Identify the blood parasite species.
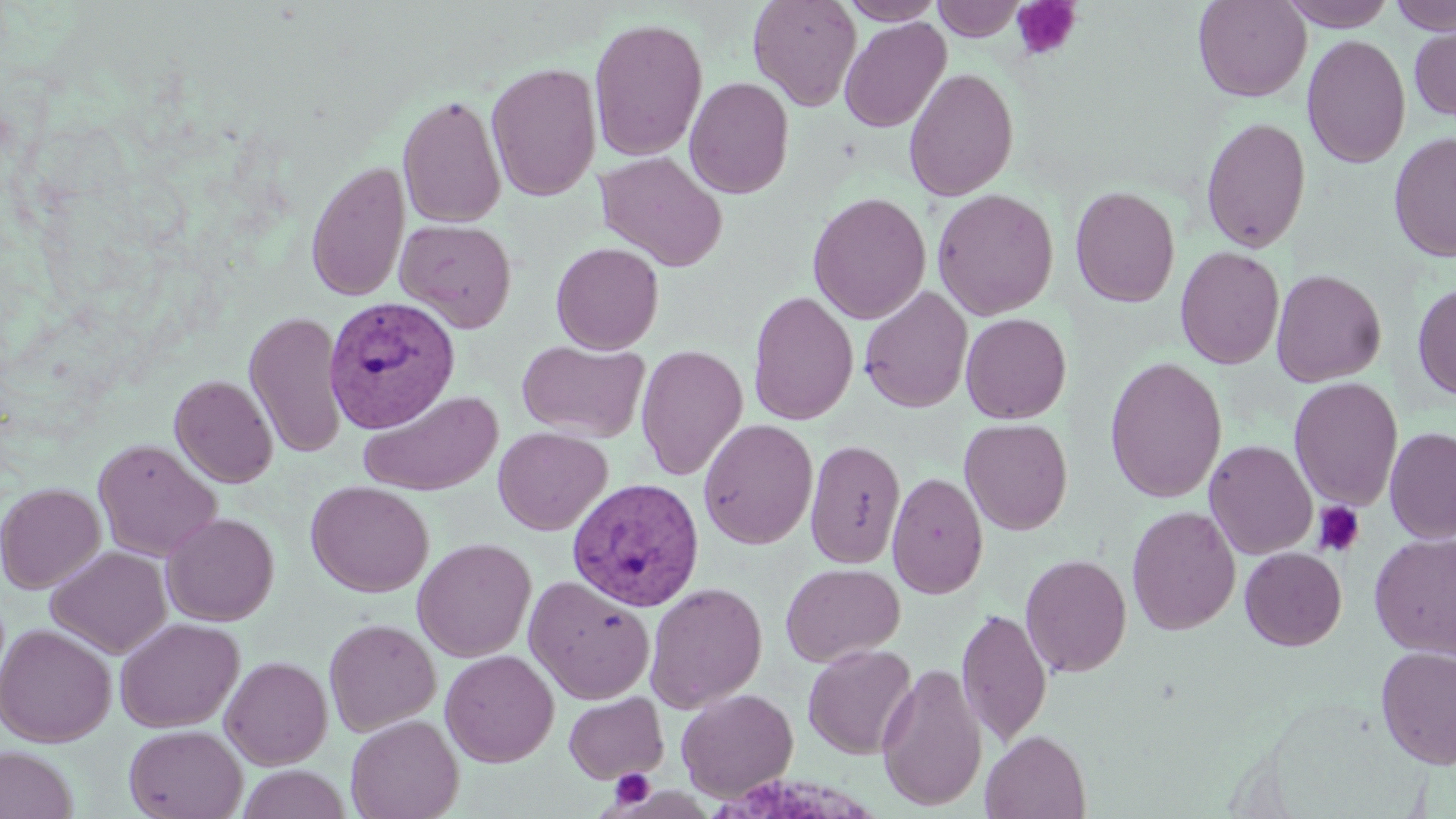
Plasmodium vivax.

{
  "modality": "light microscopy",
  "field_of_view": "single",
  "stain": "May-Grünwald-Giemsa",
  "preparation": "thin blood smear",
  "plasmodium_vivax_infected_red_blood_cell_locations": "approximate bounding boxes as [x1, y1, x2, y2] in pixels: [324, 296, 461, 434], [566, 476, 705, 612]",
  "image_size": "1456×819 pixels",
  "uninfected_red_blood_cell_locations": "approximate bounding boxes as [x1, y1, x2, y2] in pixels: [747, 0, 863, 111], [839, 0, 946, 25], [932, 0, 1027, 41], [1193, 0, 1311, 102], [1279, 0, 1397, 30], [1388, 0, 1456, 35], [839, 16, 951, 133], [589, 17, 708, 161], [1408, 23, 1456, 122], [1301, 33, 1411, 169], [487, 62, 602, 201], [903, 67, 1019, 202], [684, 76, 794, 199], [397, 93, 506, 229], [1200, 116, 1311, 253], [1388, 131, 1456, 262], [595, 151, 727, 272], [305, 160, 410, 303], [1070, 186, 1180, 307], [932, 188, 1059, 320], [808, 191, 931, 324], [395, 218, 517, 332], [550, 242, 664, 355], [1175, 246, 1285, 369], [1271, 268, 1387, 387], [1412, 281, 1456, 402], [858, 286, 973, 413], [748, 290, 859, 425], [244, 310, 348, 459], [960, 312, 1071, 424], [516, 339, 650, 442], [635, 343, 749, 482], [1104, 356, 1228, 504], [169, 374, 278, 488], [1289, 377, 1403, 510], [359, 389, 503, 496], [959, 417, 1073, 535], [698, 418, 818, 549], [1384, 426, 1456, 543], [493, 427, 612, 535], [93, 438, 222, 561], [805, 439, 906, 569], [1204, 439, 1318, 560], [887, 471, 988, 599], [0, 481, 106, 593], [305, 481, 434, 597], [1126, 505, 1241, 636], [161, 511, 279, 626], [1369, 532, 1456, 659], [412, 537, 536, 662], [46, 546, 171, 659], [1240, 547, 1347, 650], [1020, 553, 1132, 678], [780, 562, 905, 667], [524, 575, 655, 705], [644, 581, 768, 713], [957, 607, 1052, 746], [114, 617, 244, 733], [324, 617, 441, 736], [0, 624, 116, 746], [803, 643, 917, 759], [1374, 646, 1456, 769], [440, 648, 559, 767], [220, 655, 333, 770], [876, 662, 988, 811], [677, 687, 799, 802], [564, 691, 668, 783], [346, 714, 464, 819], [124, 724, 247, 819], [981, 729, 1092, 818], [0, 746, 78, 819], [235, 765, 353, 819]",
  "magnification": "1000x",
  "platelet_locations": "approximate bounding boxes as [x1, y1, x2, y2] in pixels: [1010, 0, 1082, 62], [1312, 501, 1365, 557], [610, 768, 655, 808]"
}